Describe the morphology of the red blood cells.
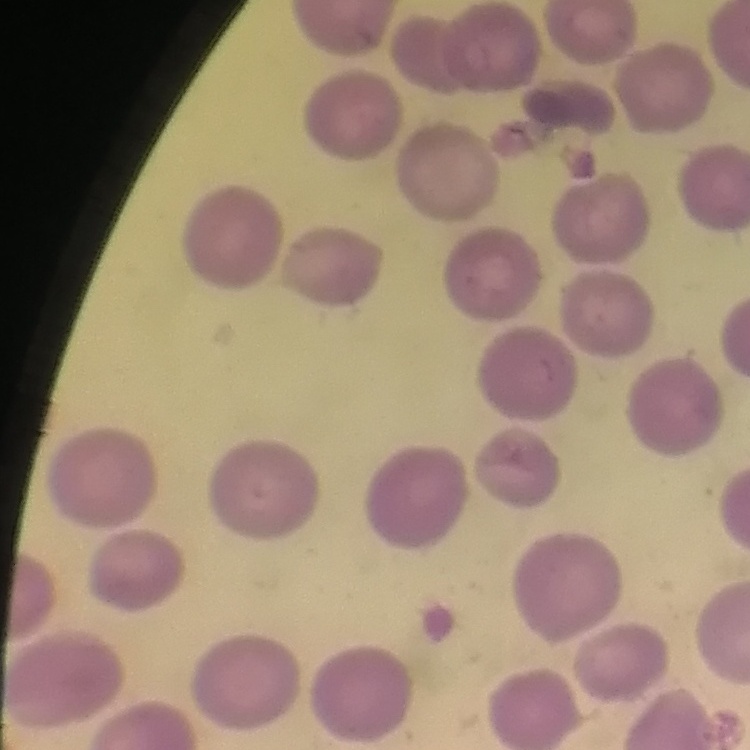
No rouleaux formation.

Summary:
  - Stain: Field's or Giemsa
  - Image type: one tile cut from a larger photomicrograph
  - Preparation: thin blood smear